Name the parasite shown.
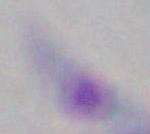

This is Toxoplasma gondii.

modality = photomicrograph
magnification = 1000x